Outline each blood parasite and name the species.
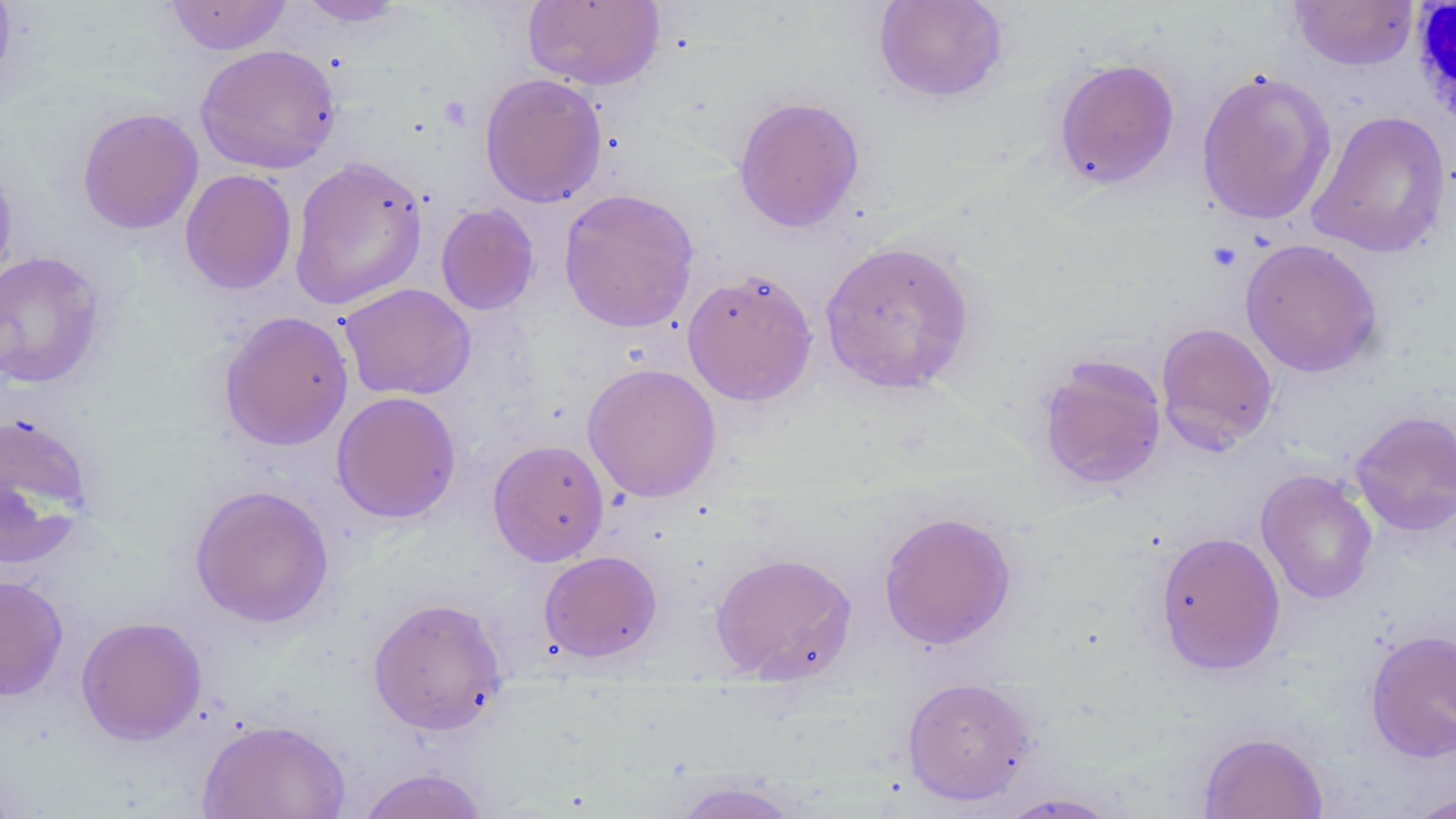

No blood parasites observed.

slide-level diagnosis = negative for blood parasites
uninfected red blood cell locations = approximate bounding boxes as (x1,y1)-(x2,y2) corner pairs in pixels: (164,0)-(293,55), (295,0)-(411,27), (873,0)-(1009,103), (0,1)-(18,95), (523,1)-(665,90), (1290,1)-(1418,71), (195,44)-(341,174), (1053,58)-(1180,190), (1196,68)-(1337,226), (479,72)-(607,208), (732,95)-(865,233), (77,107)-(203,235), (1307,110)-(1453,259), (0,156)-(18,290), (289,156)-(428,310), (180,169)-(297,295), (558,188)-(700,333), (436,203)-(540,316), (1240,238)-(1383,378), (819,240)-(977,395), (0,251)-(107,389), (682,268)-(818,407), (339,282)-(476,401), (218,310)-(354,451), (1155,322)-(1278,454), (1037,355)-(1167,492), (582,362)-(722,503), (331,391)-(461,524), (1351,410)-(1456,536), (0,411)-(96,570), (487,439)-(609,566), (1256,469)-(1378,605), (189,484)-(335,628), (878,511)-(1017,650), (1154,531)-(1286,676), (538,550)-(663,663), (710,551)-(858,684), (0,575)-(69,701), (367,596)-(508,736), (75,615)-(207,745), (1365,628)-(1456,762), (901,676)-(1038,806), (198,718)-(351,819), (1198,731)-(1328,819), (355,767)-(491,818), (667,779)-(807,818), (1401,791)-(1455,818), (995,792)-(1127,818)
magnification = 1000x
preparation = thin blood smear
white blood cell locations = approximate bounding boxes as (x1,y1)-(x2,y2) corner pairs in pixels: (1410,1)-(1456,133)
field of view = one of a larger specimen
stain = May-Grünwald-Giemsa
modality = optical microscopy
image size = 1456×819 pixels